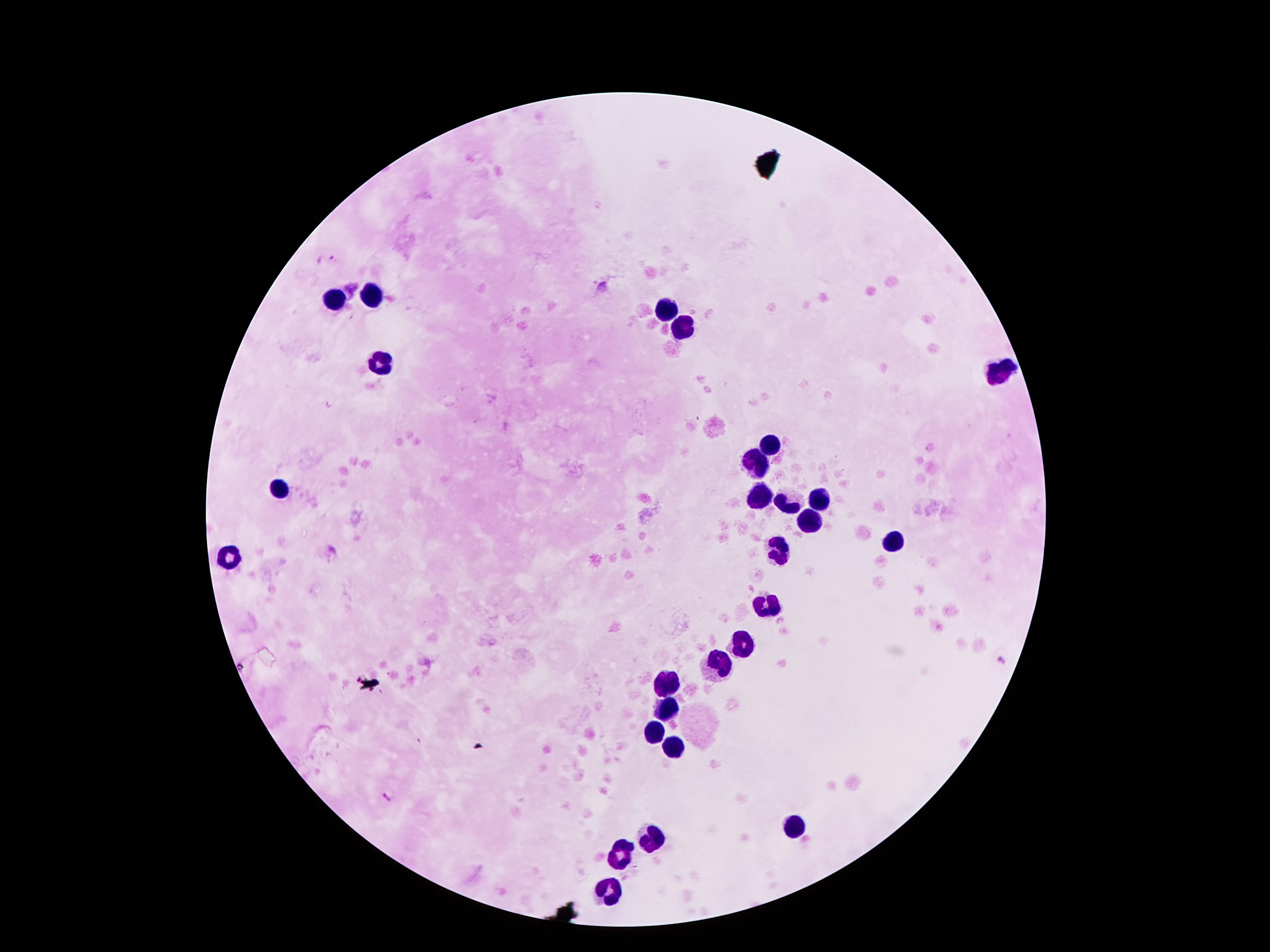
Thick blood smear. Single field of view. Giemsa-stained preparation. Patient malaria status: positive for Plasmodium falciparum. 100x magnification. Smartphone photograph taken through the microscope eyepiece. Image is 1270×952 pixels.